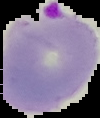
image_type: segmented cell region on a black background
preparation: thin blood film
malaria_status: parasitized
image_size: 100×118 pixels